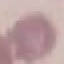

Result: no malaria parasites seen. Thin smear of blood. Photographed with a smartphone camera at the microscope eyepiece. Giemsa-stained preparation. Cell patch, automatically extracted from a larger field of view and resized to 64 × 64 pixels.